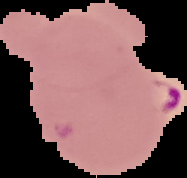 Image is 187×178 pixels. From a thin blood smear. Result: malaria parasites identified. The area outside the segmented cell region is set to black.